Report the malaria status of this cell.
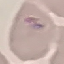

Uninfected.

capture = smartphone through the microscope eyepiece
image type = cell patch, automatically extracted from a larger field of view and resized to 64 × 64 pixels
stain = Giemsa
preparation = thin smear